Outline each blood parasite and name the species.
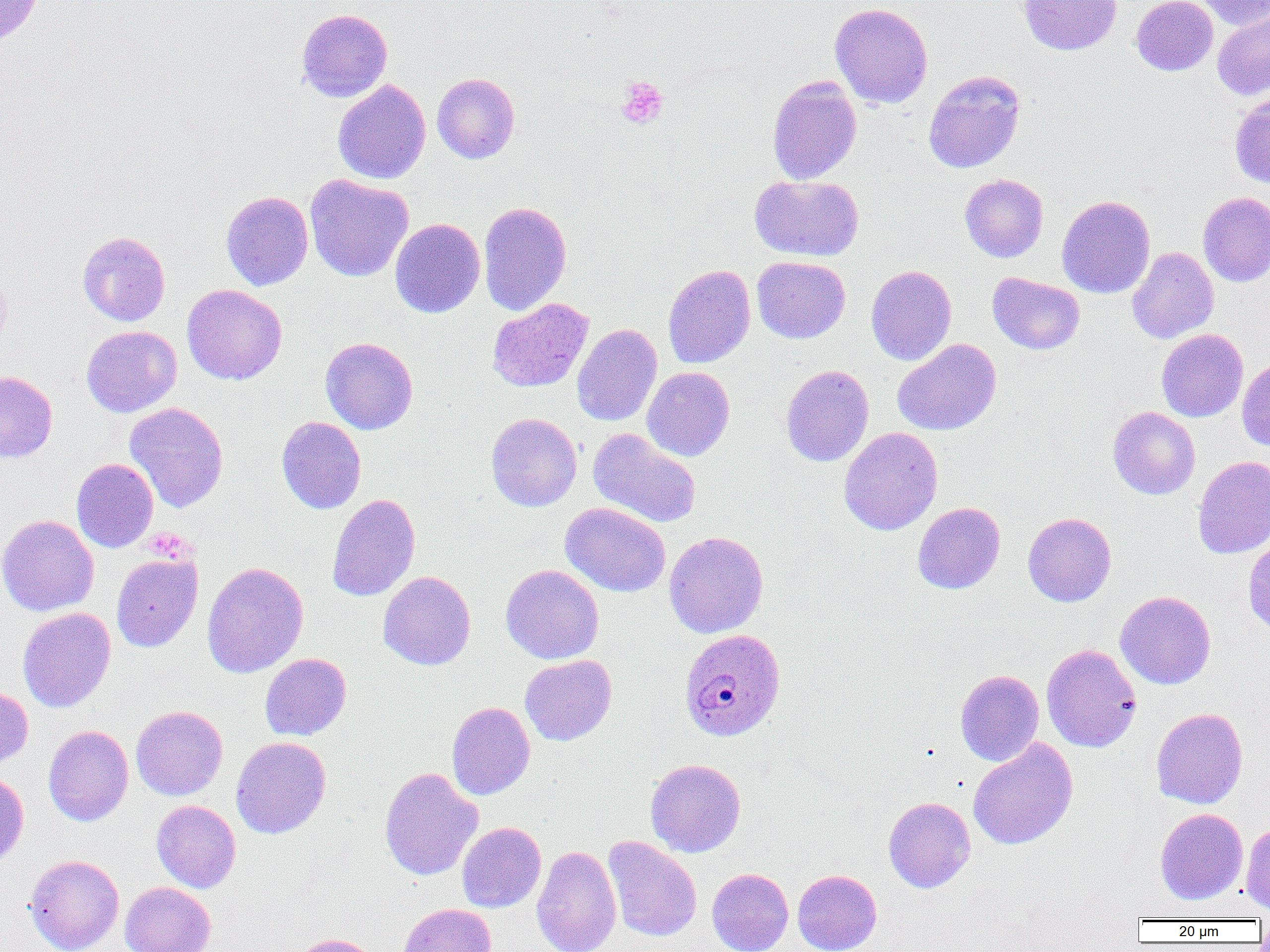

Approximate bounding boxes as [x1, y1, x2, y2] in pixels.
Plasmodium malariae-infected red blood cells: [679, 629, 786, 742].
No Plasmodium falciparum, Plasmodium ovale, Plasmodium vivax, Babesia divergens, or Trypanosoma brucei observed.

slide-level diagnosis = Plasmodium malariae
magnification = 1000x
field of view = one of a larger specimen
image size = 1270×952 pixels
modality = optical microscopy
uninfected red blood cell locations = approximate bounding boxes as [x1, y1, x2, y2] in pixels: [0, 0, 46, 50], [1018, 0, 1122, 56], [1131, 0, 1218, 75], [1198, 0, 1270, 30], [830, 3, 933, 108], [296, 8, 393, 102], [1212, 10, 1270, 101], [923, 70, 1026, 173], [432, 72, 520, 164], [767, 76, 862, 185], [332, 80, 431, 184], [1229, 93, 1270, 188], [305, 174, 413, 282], [750, 174, 864, 262], [959, 174, 1048, 262], [220, 191, 313, 291], [1198, 192, 1270, 286], [1056, 195, 1155, 298], [478, 201, 572, 316], [390, 218, 485, 318], [77, 231, 170, 326], [1127, 246, 1219, 344], [752, 256, 850, 344], [663, 264, 756, 369], [866, 265, 956, 366], [0, 271, 11, 352], [987, 273, 1085, 354], [182, 284, 287, 385], [487, 298, 593, 393], [572, 323, 662, 426], [81, 325, 182, 417], [1156, 329, 1248, 422], [320, 337, 418, 435], [892, 339, 1002, 436], [1237, 359, 1270, 452], [780, 364, 874, 467], [642, 367, 735, 461], [0, 371, 58, 463], [124, 402, 229, 513], [1108, 406, 1200, 499], [485, 412, 582, 511], [276, 416, 366, 514], [838, 427, 943, 535], [588, 428, 702, 528], [1192, 455, 1270, 559], [71, 458, 158, 552], [327, 494, 421, 601], [560, 502, 671, 597], [912, 502, 1006, 594], [1022, 512, 1117, 607], [0, 515, 99, 616], [664, 531, 769, 638], [1243, 536, 1270, 637], [111, 553, 203, 652], [201, 562, 309, 678], [500, 564, 604, 664], [378, 571, 476, 670], [1115, 591, 1216, 689], [18, 607, 116, 712], [1041, 644, 1142, 752], [259, 653, 351, 741], [519, 655, 617, 746], [955, 669, 1044, 766], [0, 685, 33, 769], [447, 702, 535, 800], [131, 706, 228, 800], [1151, 707, 1248, 808], [43, 725, 134, 826], [231, 736, 331, 839], [968, 737, 1078, 850], [645, 758, 746, 857], [379, 767, 483, 881], [0, 769, 28, 870], [883, 796, 975, 893], [151, 800, 241, 893], [1155, 808, 1248, 904], [457, 822, 546, 912], [1241, 822, 1270, 915], [603, 836, 702, 942], [532, 845, 622, 952], [25, 854, 124, 952], [707, 867, 793, 952], [792, 869, 882, 952], [120, 882, 216, 952], [398, 903, 496, 952], [290, 933, 382, 952]
preparation = thin blood smear
platelet locations = approximate bounding boxes as [x1, y1, x2, y2] in pixels: [615, 76, 669, 129]